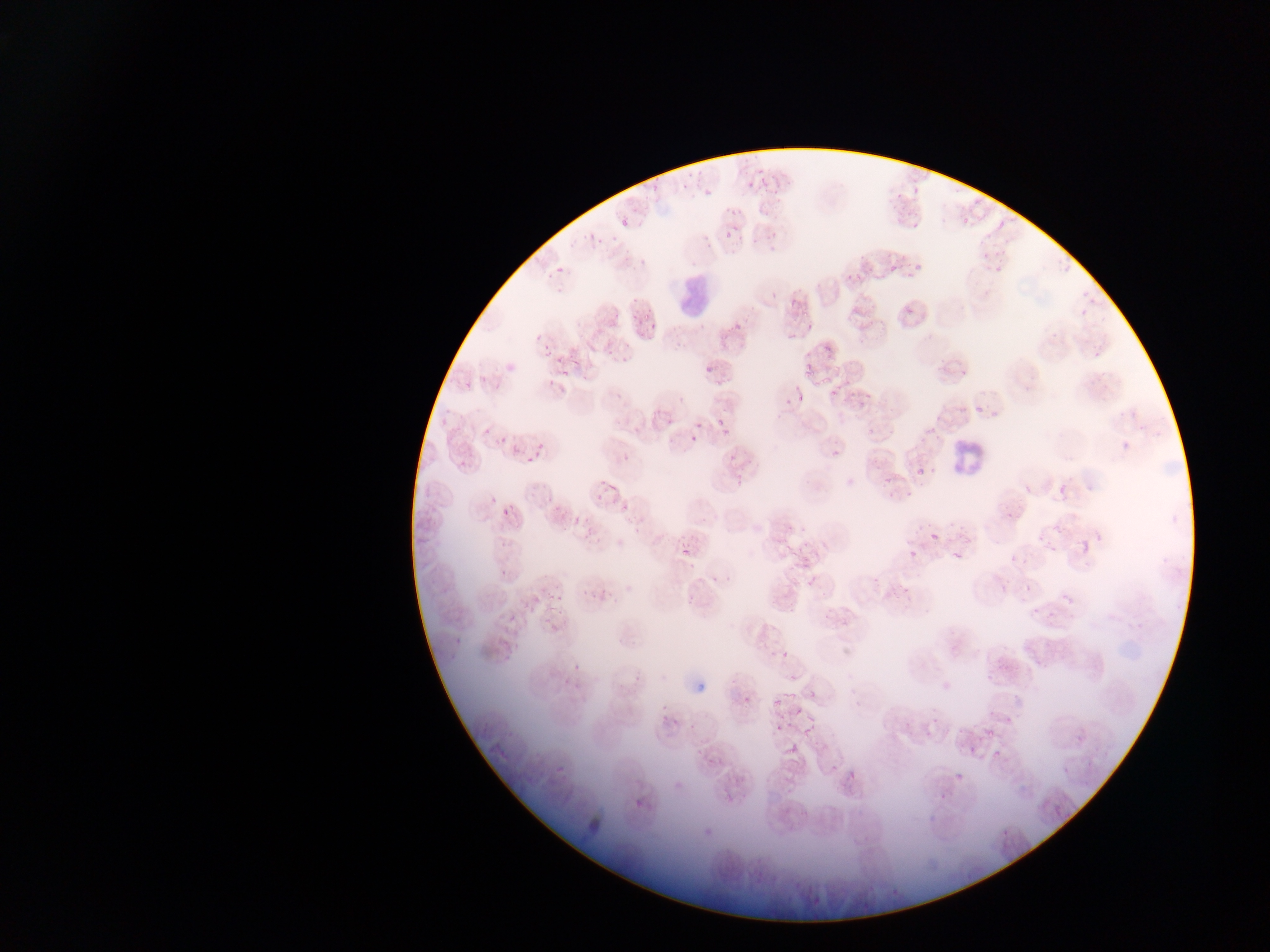
Approximate bounding boxes as (left, top, right, bottom) in pixels.
Summary:
  - Artifact (stain precipitate or debris) locations: (684, 672, 717, 694)
  - Leukocyte locations: (666, 265, 723, 321), (949, 434, 994, 474)
  - Plasmodium parasite locations: (724, 230, 732, 238), (554, 264, 565, 274), (889, 264, 899, 272), (553, 352, 565, 365), (703, 362, 718, 372), (803, 364, 815, 378), (956, 364, 971, 380), (477, 372, 488, 383), (818, 378, 828, 387), (460, 380, 476, 391), (828, 391, 839, 401), (796, 393, 805, 405), (857, 398, 867, 410), (972, 402, 991, 412), (716, 416, 723, 426), (437, 417, 449, 428), (695, 420, 704, 433), (482, 425, 492, 435), (866, 428, 874, 440), (720, 430, 730, 438), (498, 433, 510, 441), (688, 434, 698, 443), (536, 439, 547, 450), (508, 442, 522, 453), (531, 448, 540, 460), (826, 449, 846, 460), (723, 453, 737, 464), (457, 456, 468, 467), (524, 456, 535, 466), (917, 468, 928, 479), (731, 472, 746, 487), (1057, 477, 1074, 496), (606, 485, 619, 493), (1024, 485, 1034, 495), (595, 492, 604, 502), (488, 494, 499, 505), (509, 504, 520, 512), (498, 506, 509, 515), (1004, 509, 1017, 519), (930, 527, 948, 541), (1038, 532, 1047, 541), (616, 537, 625, 548), (1081, 538, 1091, 551), (1049, 542, 1060, 553), (685, 546, 695, 559), (950, 548, 967, 567), (908, 549, 919, 559), (1007, 552, 1017, 563), (1021, 554, 1035, 563), (499, 567, 508, 576), (708, 567, 722, 584), (871, 576, 880, 585), (807, 579, 815, 588), (999, 582, 1008, 592), (1024, 582, 1032, 594), (548, 589, 562, 599), (581, 590, 589, 595), (1063, 593, 1075, 605), (592, 594, 600, 600), (1029, 608, 1040, 617), (1043, 611, 1057, 619), (507, 614, 517, 624), (550, 620, 560, 631), (510, 631, 522, 648), (451, 635, 462, 643), (780, 651, 789, 661), (571, 660, 582, 669), (942, 681, 952, 691), (807, 687, 816, 698), (785, 691, 795, 702), (774, 697, 782, 705), (794, 707, 803, 715), (988, 707, 999, 718), (806, 711, 818, 724), (661, 714, 673, 722), (671, 714, 683, 728), (1005, 715, 1012, 726), (779, 717, 791, 728), (801, 724, 819, 734), (987, 731, 996, 740), (1075, 733, 1086, 744), (968, 739, 980, 754), (787, 745, 797, 754), (992, 748, 1003, 762), (831, 765, 838, 773), (555, 766, 564, 774), (1062, 766, 1070, 774), (955, 771, 965, 781), (674, 780, 682, 790), (940, 784, 950, 797), (632, 796, 646, 809), (1054, 803, 1070, 817), (703, 818, 723, 837), (999, 825, 1013, 836) | approximate (x, y) pixel centers of objects too small to bound: (554, 607)
  - Preparation: thin blood smear
  - Country: Ghana
  - Image size: 1270×952 pixels
  - Field of view: single
  - Capture: mobile-phone photograph through a microscope